Give the location of every parasitized red blood cell.
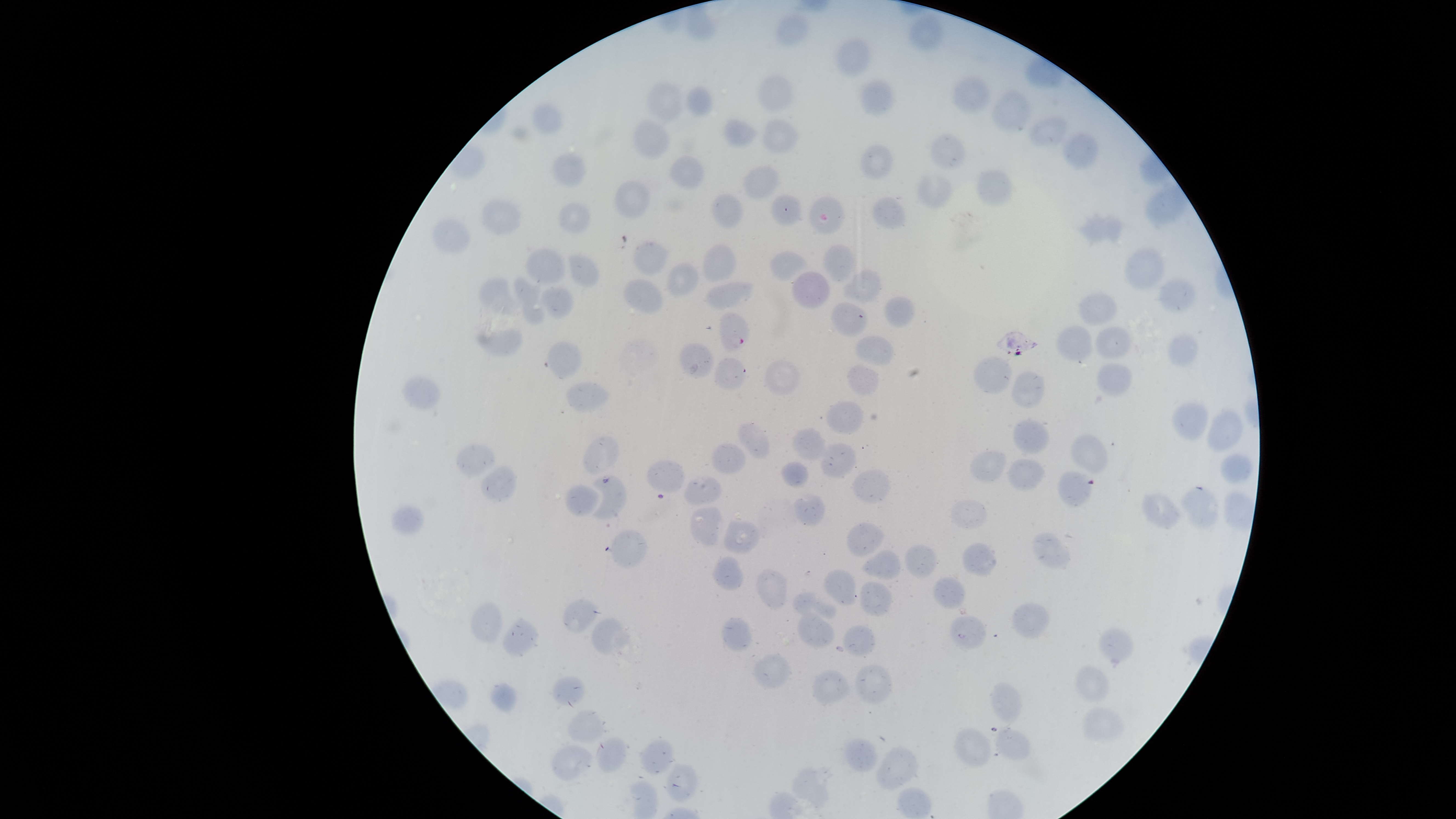

Approximate bounding boxes as [left, top, right, bottom] in pixels.
Parasitized red blood cells: [809, 196, 845, 235], [719, 310, 751, 352].

Approximate bounding boxes as [left, top, right, bottom] in pixels.
Summary:
  - Uninfected red blood cells: [906, 13, 945, 52], [775, 14, 808, 47], [835, 38, 872, 78], [758, 73, 795, 114], [951, 74, 991, 114], [859, 77, 894, 118], [645, 81, 683, 122], [685, 85, 713, 118], [992, 90, 1031, 135], [530, 103, 563, 134], [1028, 116, 1068, 149], [722, 118, 759, 148], [763, 118, 799, 154], [631, 119, 670, 161], [930, 132, 966, 171], [1063, 133, 1098, 170], [859, 144, 894, 180], [551, 151, 587, 188], [669, 155, 706, 190], [743, 165, 781, 200], [975, 169, 1013, 205], [916, 173, 953, 209], [613, 180, 650, 218], [712, 193, 744, 229], [769, 194, 802, 228], [872, 196, 906, 230], [480, 200, 522, 236], [558, 201, 591, 234], [1075, 212, 1124, 245], [432, 217, 471, 257], [632, 240, 671, 277], [703, 244, 737, 283], [823, 244, 856, 282], [525, 246, 566, 285], [1125, 248, 1164, 290], [770, 249, 807, 282], [568, 253, 600, 288], [666, 262, 699, 297], [842, 269, 883, 303], [791, 271, 830, 309], [513, 276, 545, 324], [477, 277, 521, 316], [1159, 278, 1196, 312], [623, 279, 663, 313], [706, 281, 754, 311], [539, 286, 575, 318], [1079, 292, 1117, 326], [884, 296, 916, 328], [830, 301, 868, 337], [1056, 325, 1093, 361], [1095, 326, 1132, 360], [476, 328, 523, 358], [1168, 335, 1198, 368], [855, 336, 894, 366], [547, 341, 582, 378], [679, 342, 714, 378], [973, 356, 1013, 395], [714, 357, 747, 390], [764, 359, 801, 395], [1096, 363, 1132, 397], [846, 364, 879, 396], [1010, 371, 1047, 410], [403, 376, 442, 412], [566, 381, 611, 413], [826, 401, 864, 435], [1172, 401, 1208, 443], [1205, 409, 1244, 452], [1012, 419, 1049, 455], [737, 423, 771, 460], [792, 426, 831, 462], [1070, 434, 1108, 475], [583, 435, 620, 476], [711, 442, 747, 474], [820, 443, 858, 479], [455, 444, 495, 478], [969, 451, 1007, 483], [1220, 454, 1252, 484], [646, 459, 685, 492], [1006, 459, 1045, 493], [781, 461, 808, 488], [481, 466, 518, 504], [851, 469, 890, 504], [590, 474, 626, 520], [683, 476, 722, 506], [566, 483, 601, 516], [1181, 486, 1219, 530], [1141, 492, 1181, 530], [794, 494, 826, 526], [949, 500, 987, 529], [392, 505, 424, 536], [690, 506, 723, 546], [724, 517, 761, 555], [846, 522, 885, 558], [608, 530, 648, 570], [1032, 532, 1071, 569], [962, 542, 998, 576], [904, 544, 938, 579], [861, 549, 902, 580], [712, 555, 744, 591], [756, 569, 787, 610], [824, 569, 857, 606], [932, 577, 966, 610], [860, 581, 894, 617], [791, 592, 837, 620], [563, 599, 600, 634], [470, 601, 503, 644], [1012, 601, 1051, 639], [796, 614, 835, 648], [950, 614, 986, 649], [502, 615, 539, 658], [592, 617, 631, 657], [721, 617, 753, 652], [843, 625, 876, 656], [1098, 627, 1135, 664], [753, 653, 791, 689], [854, 664, 893, 704], [1075, 665, 1110, 704], [810, 670, 851, 706], [553, 676, 586, 707], [489, 681, 517, 714], [991, 682, 1022, 724], [1082, 706, 1125, 742], [567, 709, 605, 743], [991, 727, 1032, 761], [953, 728, 992, 768], [595, 737, 629, 773], [842, 737, 878, 773], [640, 738, 674, 775], [551, 745, 593, 782], [875, 746, 919, 790], [665, 763, 697, 803], [792, 767, 834, 812]
  - Preparation: thin blood film
  - Visible region: circular
  - Species: Plasmodium falciparum
  - Stain: Giemsa
  - Field of view: single
  - Image size: 1456×819 pixels
  - Capture: smartphone photograph through the microscope eyepiece